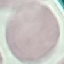

Summary:
  - Result: negative for malaria parasites
  - Image type: cell patch, automatically extracted from a larger field of view and resized to 64 × 64 pixels
  - Preparation: thin blood smear
  - Stain: Giemsa
  - Capture: smartphone through the microscope eyepiece